Report the malaria status of this cell.
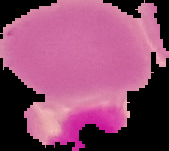

It is uninfected.

preparation = thin blood film
image size = 169×151 pixels
image type = segmented cell region on a black background